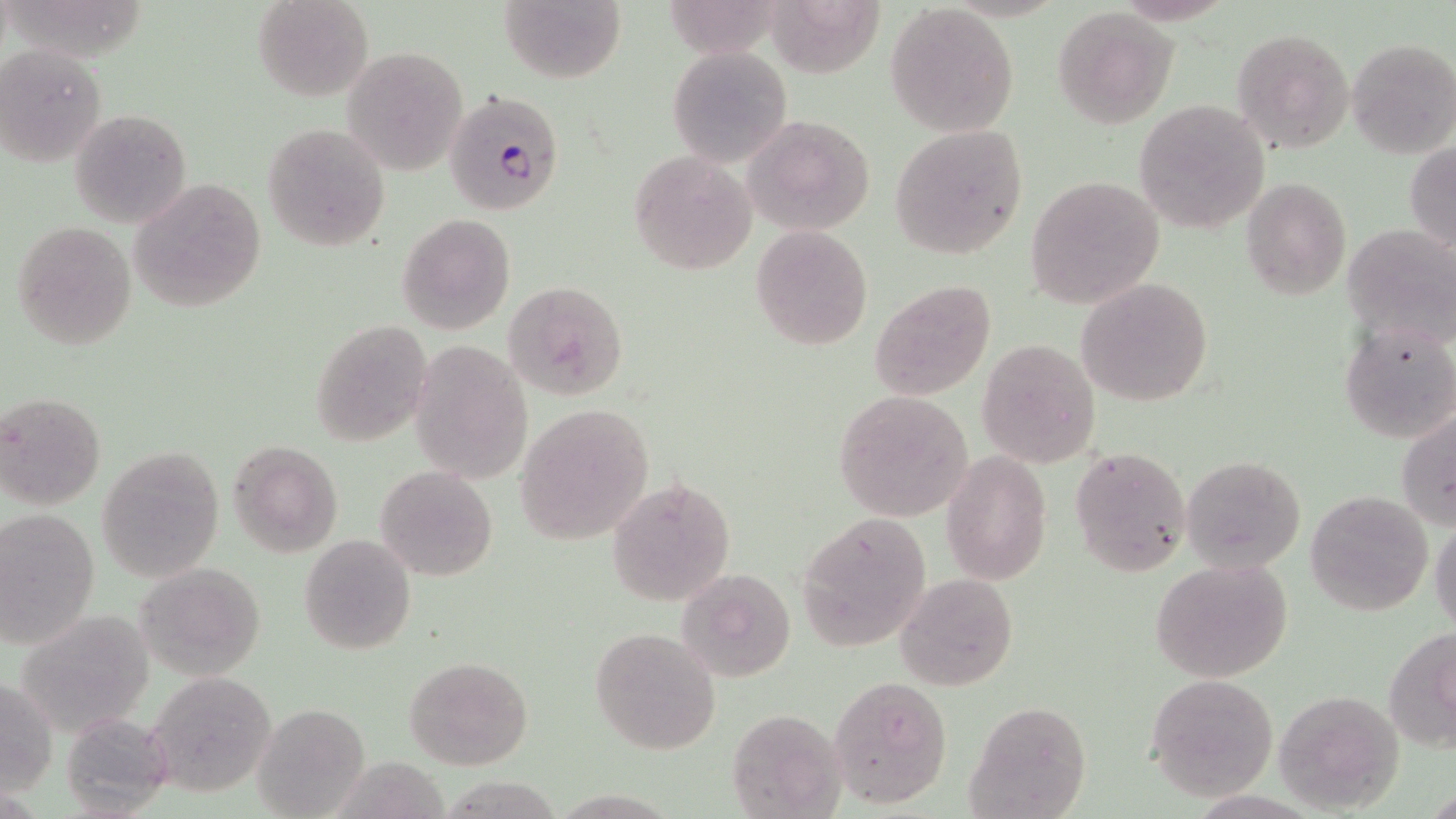

Approximate bounding boxes as (x1, y1, x2, y2) in pixels. Plasmodium falciparum-infected red blood cell locations: (444, 89, 566, 217). Uninfected red blood cell locations: (252, 0, 372, 101), (498, 0, 625, 84), (885, 4, 1020, 138), (1052, 7, 1177, 127), (1232, 27, 1354, 154), (1346, 37, 1455, 157), (1, 45, 107, 168), (667, 45, 795, 167), (342, 46, 469, 174), (1134, 101, 1270, 234), (68, 106, 193, 230), (744, 114, 876, 237), (263, 122, 392, 251), (889, 125, 1028, 258), (1405, 144, 1456, 253), (628, 151, 758, 275), (1025, 175, 1167, 308), (129, 178, 266, 311), (1241, 178, 1351, 299), (397, 212, 516, 335), (11, 220, 139, 349), (1342, 222, 1456, 349), (750, 225, 873, 349), (1076, 276, 1214, 407), (870, 279, 996, 399), (505, 281, 629, 401), (310, 319, 433, 446), (1338, 320, 1456, 445), (976, 338, 1101, 468), (410, 339, 534, 483), (832, 391, 973, 520), (0, 392, 107, 511), (515, 404, 654, 546), (1397, 408, 1456, 530), (227, 440, 342, 556), (96, 444, 224, 581), (1070, 445, 1193, 579), (942, 451, 1052, 585), (1182, 455, 1305, 573), (375, 465, 496, 582), (608, 477, 736, 606), (1306, 490, 1433, 616), (0, 507, 100, 649), (795, 512, 931, 651), (1429, 519, 1456, 638), (299, 535, 416, 655), (1150, 558, 1295, 684), (136, 561, 265, 680), (676, 568, 798, 681), (896, 573, 1019, 691), (590, 626, 722, 755), (1384, 628, 1456, 754), (404, 655, 533, 769), (144, 671, 278, 799), (1145, 674, 1278, 800), (830, 677, 953, 808), (1, 678, 56, 795), (1270, 688, 1402, 813), (965, 701, 1092, 818), (254, 702, 370, 819), (726, 708, 844, 816), (60, 713, 175, 816). Slide-level diagnosis: Plasmodium falciparum. Optical microscopy. One field of a larger specimen. Thin blood film. Image is 1456×819 pixels. Captured at 1000x magnification. May-Grünwald-Giemsa-stained preparation.